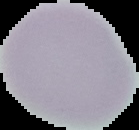

Malaria status: uninfected. From a thin blood smear. The area outside the segmented cell region is set to black. Image is 139×130 pixels.